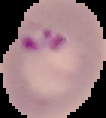
Image is 106×118 pixels. Cell region segmented out of the field of view; the surrounding area is masked to black. Result: Plasmodium parasites identified. From a thin blood smear.